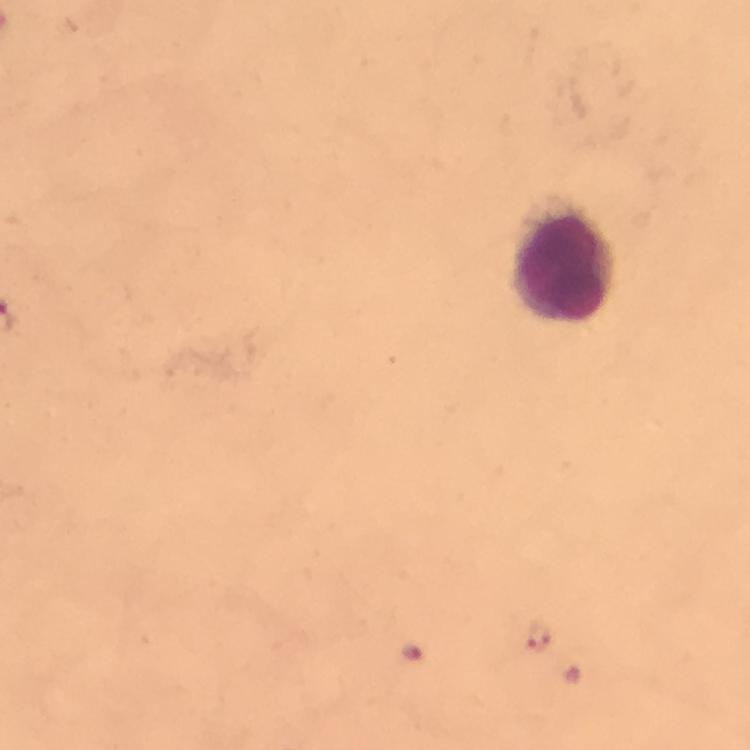

{
  "cropped_from": "a single field of view",
  "preparation": "thick blood smear",
  "image_size": "750×750 pixels",
  "immersion_oil": "applied",
  "stain": "Giemsa",
  "capture": "smartphone mounted on the microscope",
  "plasmodium_parasite_locations": "approximate centers as {x, y} in pixels: {539, 635}, {413, 654}",
  "leukocyte_locations": "approximate centers as {x, y} in pixels: {563, 260}",
  "magnification": "100x",
  "context": "from a malaria diagnostic workup"
}